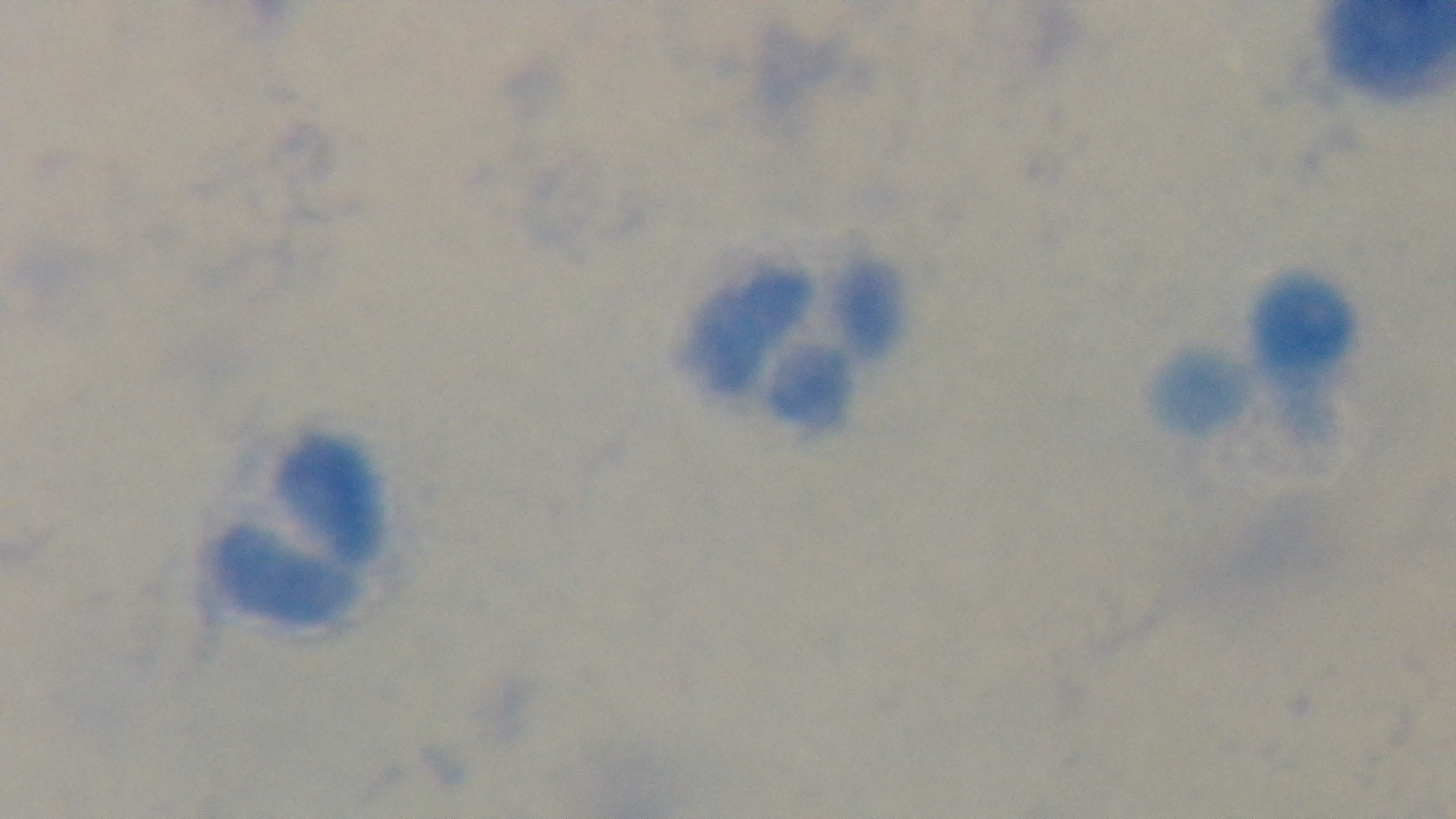
Summary:
  - Malaria status: uninfected
  - Preparation: thick smear
  - Objective: 100x oil immersion
  - Modality: light microscopy
  - Stain: Giemsa
  - Field of view: one from the slide
  - Capture: mounted 4K digital camera